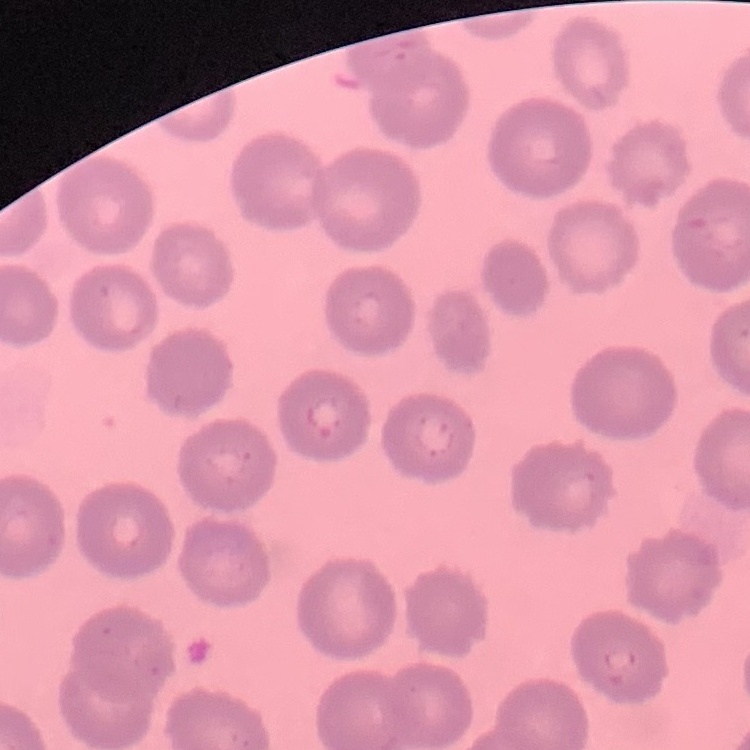
The red blood cells show no rouleaux formation. Square crop of a larger photomicrograph. Field's or Giemsa stain. Thin blood film.